Assess the morphology of the red blood cells.
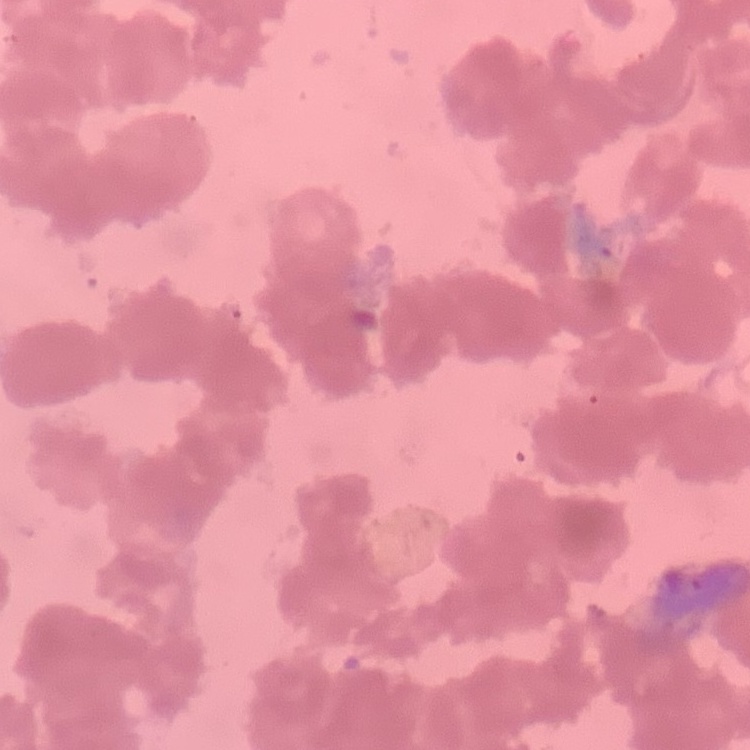

Rouleaux formation.

Field's or Giemsa stain. One tile cut from a larger photomicrograph. Thin blood smear.